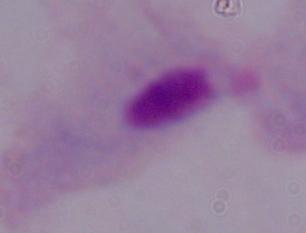

modality: photomicrograph
magnification: 1000x
identification: trichomonad